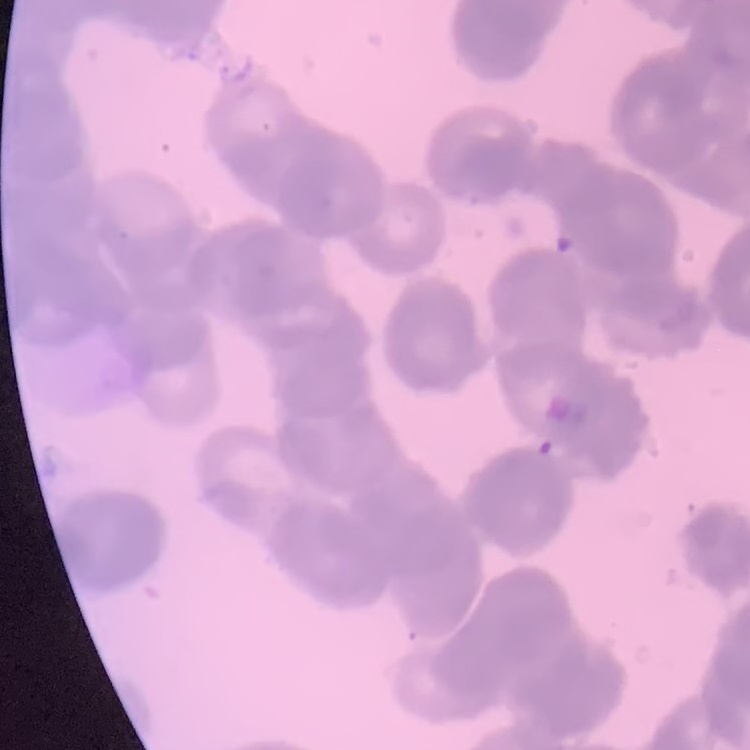

The red blood cells exhibit rouleaux formation. One tile cut from a larger photomicrograph. Thin blood film. Stained with either Field's or Giemsa.